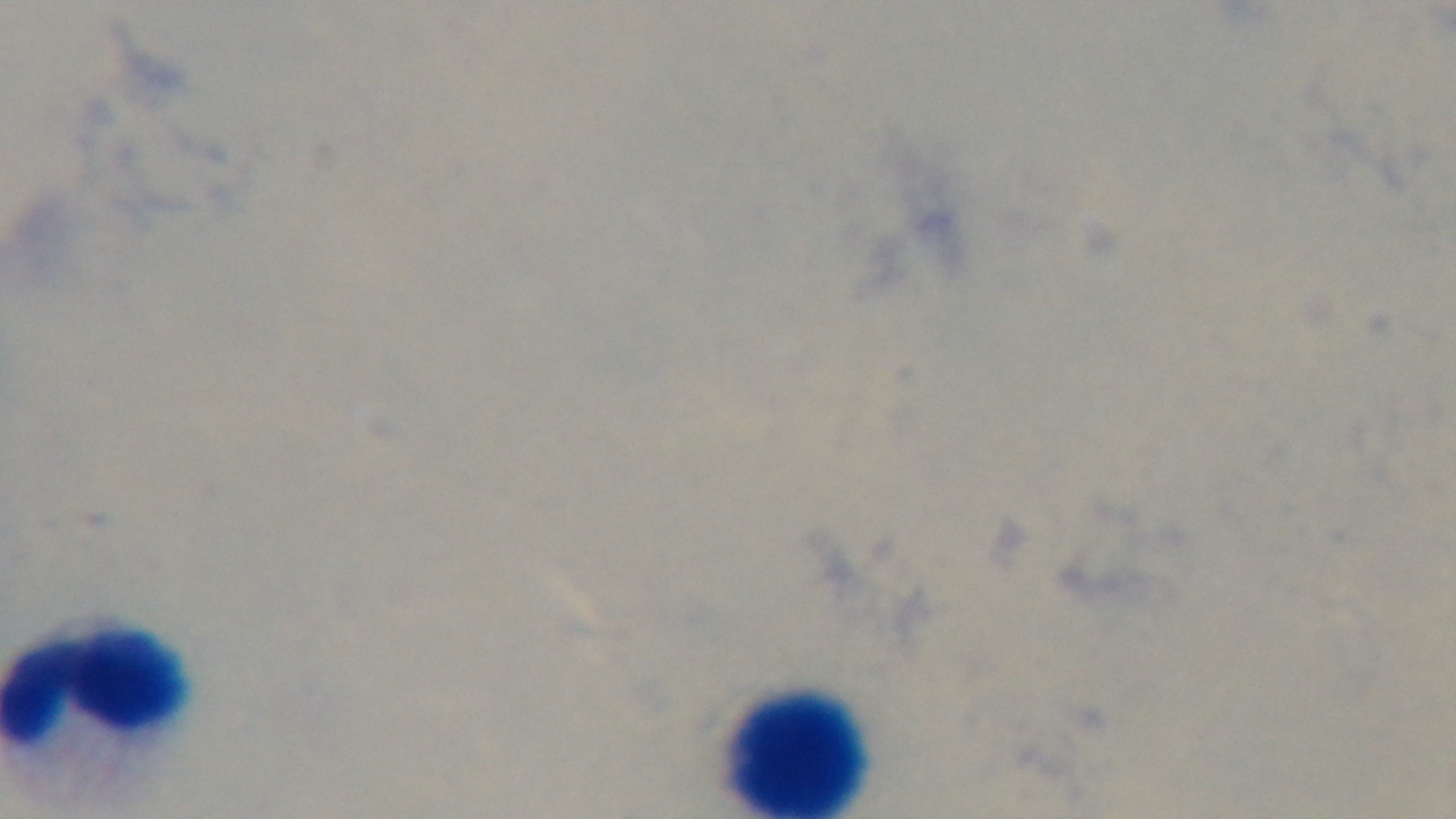

Summary:
  - Malaria status: uninfected
  - Preparation: thick
  - Capture: mounted 4K digital camera
  - Field of view: single
  - Modality: light microscopy
  - Stain: Giemsa
  - Objective: 100x oil immersion